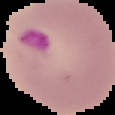

Summary:
  - Malaria status: parasitized
  - Preparation: thin blood film
  - Image type: segmented cell region with the area outside set to black
  - Image size: 115×115 pixels